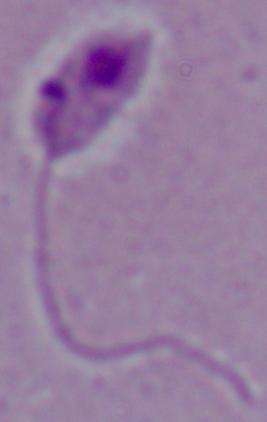
Summary:
  - Modality: photomicrograph
  - Magnification: 1000x
  - Identification: Leishmania